Give the position of every malaria parasite.
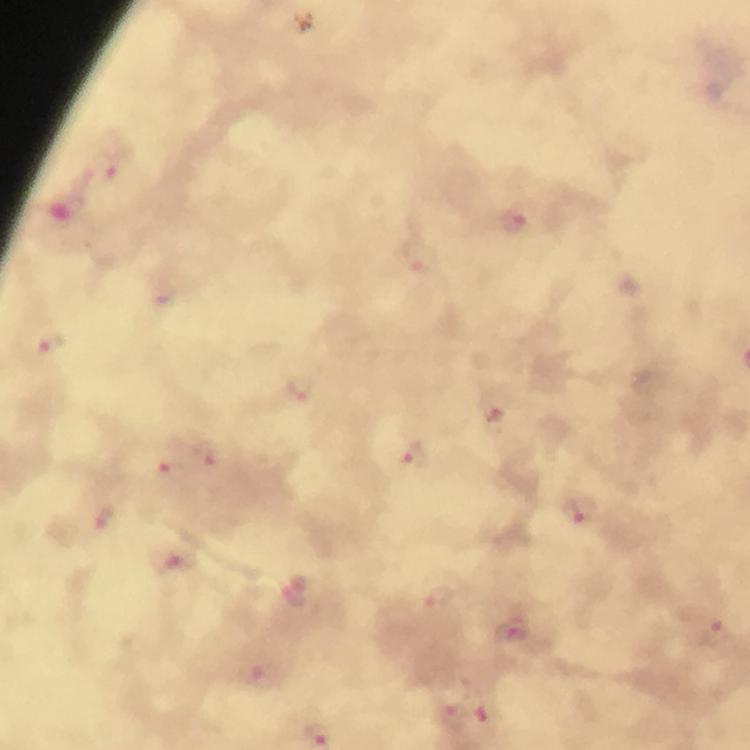

Approximate object centers, in pixels from the top-left corner.
Malaria parasites: (x=107, y=166), (x=515, y=219), (x=420, y=255), (x=52, y=344), (x=301, y=388), (x=493, y=407), (x=414, y=455), (x=204, y=456), (x=172, y=472), (x=579, y=510), (x=103, y=518), (x=175, y=562), (x=296, y=593), (x=437, y=598), (x=513, y=631), (x=716, y=633), (x=259, y=677), (x=456, y=716).

cropped from = a single field of view
immersion oil = used
capture = smartphone camera through the microscope
context = from a diagnostic examination for malaria
image size = 750×750 pixels
preparation = thick blood film
stain = Giemsa
magnification = 100x